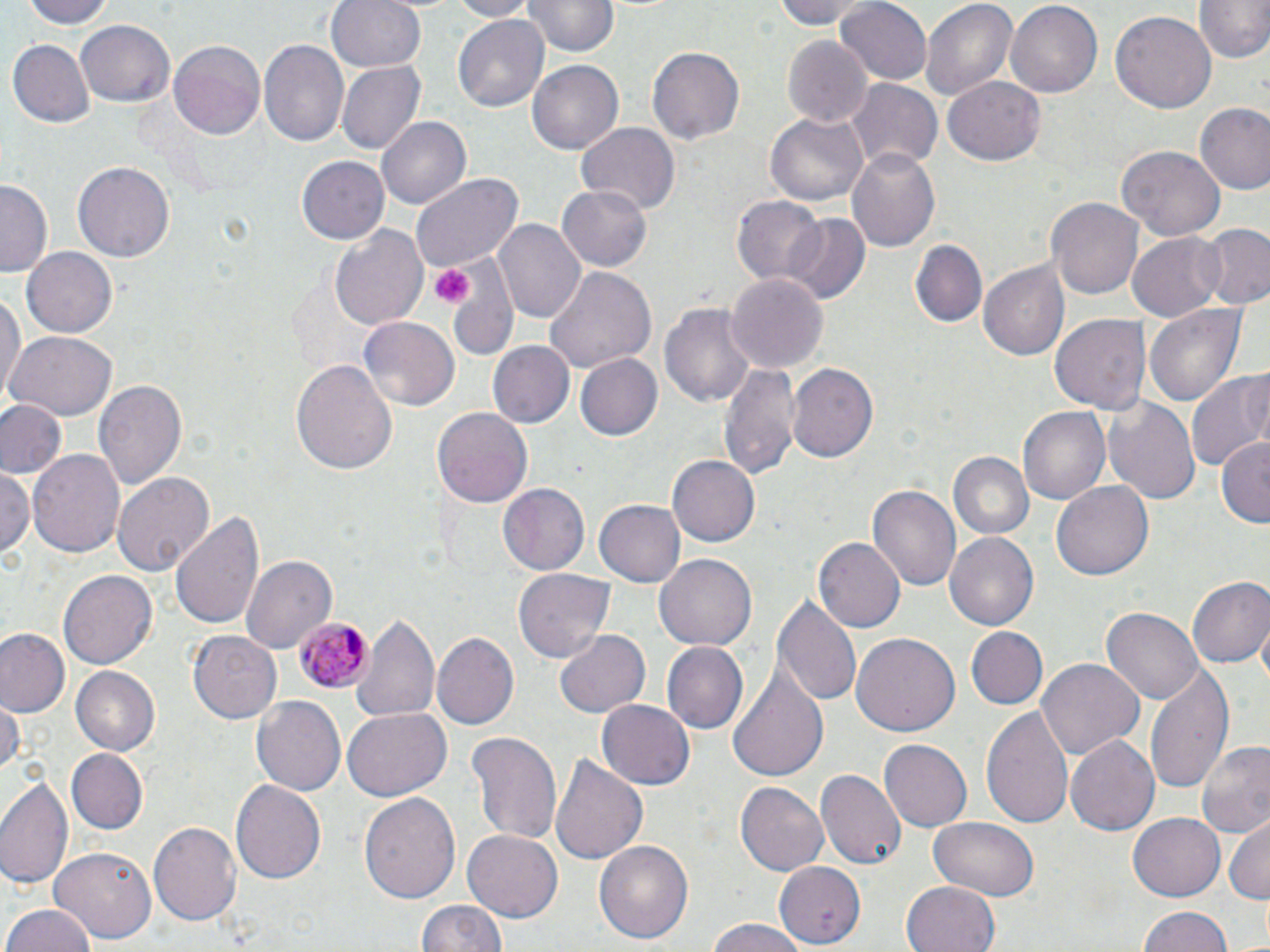

Summary:
  - Coordinate format: approximate bounding boxes as [x1, y1, x2, y2] in pixels
  - Plasmodium malariae-infected red blood cell locations: [295, 614, 373, 695]
  - Uninfected red blood cell locations: [21, 0, 118, 30], [326, 0, 427, 73], [446, 0, 535, 19], [523, 0, 618, 59], [776, 0, 880, 31], [918, 0, 1019, 104], [1191, 0, 1270, 64], [834, 1, 931, 86], [1006, 1, 1102, 95], [1112, 10, 1216, 115], [452, 11, 550, 109], [74, 17, 174, 108], [258, 38, 349, 147], [782, 38, 871, 126], [7, 39, 96, 128], [168, 40, 265, 144], [645, 46, 744, 146], [528, 60, 624, 155], [337, 61, 427, 155], [942, 76, 1045, 167], [847, 79, 941, 173], [1194, 104, 1269, 197], [766, 107, 868, 205], [377, 116, 471, 209], [577, 124, 680, 215], [1118, 143, 1225, 241], [845, 145, 943, 254], [296, 156, 390, 246], [73, 160, 176, 262], [412, 173, 525, 274], [0, 180, 51, 276], [558, 182, 655, 272], [732, 195, 828, 288], [1049, 195, 1146, 300], [780, 213, 871, 304], [494, 217, 585, 322], [1198, 223, 1270, 308], [328, 224, 430, 334], [1127, 230, 1227, 322], [910, 238, 988, 327], [22, 247, 118, 340], [445, 253, 518, 355], [977, 262, 1069, 362], [544, 263, 656, 373], [725, 271, 829, 375], [0, 286, 26, 408], [660, 298, 756, 410], [1146, 302, 1247, 407], [1051, 315, 1151, 417], [359, 317, 460, 411], [7, 332, 118, 420], [487, 341, 575, 430], [575, 354, 661, 440], [291, 358, 398, 475], [718, 359, 800, 480], [786, 359, 878, 462], [1186, 366, 1270, 476], [92, 382, 186, 495], [1106, 398, 1200, 506], [0, 400, 66, 480], [1019, 406, 1112, 505], [432, 407, 533, 510], [1216, 435, 1270, 529], [28, 449, 126, 561], [946, 452, 1033, 540], [669, 453, 760, 547], [113, 469, 215, 574], [0, 470, 33, 562], [1053, 480, 1153, 580], [499, 483, 590, 575], [867, 483, 960, 595], [595, 500, 685, 586], [170, 510, 265, 633], [944, 531, 1039, 633], [815, 538, 905, 632], [654, 551, 757, 648], [240, 555, 337, 655], [59, 570, 157, 670], [515, 570, 614, 663], [1185, 574, 1269, 671], [775, 592, 864, 709], [1102, 607, 1203, 705], [353, 611, 439, 724], [964, 627, 1048, 710], [553, 629, 652, 719], [0, 630, 69, 718], [188, 630, 281, 723], [433, 631, 518, 728], [851, 632, 961, 736], [662, 642, 747, 734], [1036, 658, 1141, 762], [1146, 663, 1233, 794], [72, 666, 161, 756], [729, 669, 829, 781], [252, 697, 344, 794], [0, 700, 22, 775], [597, 701, 692, 789], [982, 703, 1075, 831], [342, 706, 450, 801], [467, 730, 562, 848], [1066, 735, 1164, 835], [1194, 737, 1270, 842], [880, 740, 972, 832], [64, 748, 147, 835], [550, 753, 649, 865], [817, 769, 907, 872], [1, 772, 74, 894], [230, 779, 328, 887], [736, 782, 828, 875], [359, 791, 462, 905], [1127, 812, 1225, 902], [1225, 815, 1269, 903], [148, 817, 243, 924], [927, 819, 1041, 900], [462, 827, 563, 920], [595, 839, 695, 944], [52, 847, 155, 945], [773, 863, 865, 945], [901, 881, 1003, 952], [413, 898, 509, 952], [1, 906, 97, 952], [1136, 906, 1233, 952], [701, 920, 815, 952]
  - Platelet locations: [429, 260, 471, 307]
  - Slide-level diagnosis: Plasmodium malariae
  - Stain: May-Grünwald-Giemsa
  - Preparation: thin blood smear
  - Modality: light microscopy
  - Field of view: one of a larger specimen
  - Image size: 1270×952 pixels
  - Magnification: 1000x